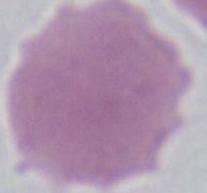

modality: photomicrograph
identification: erythrocyte
magnification: 1000x